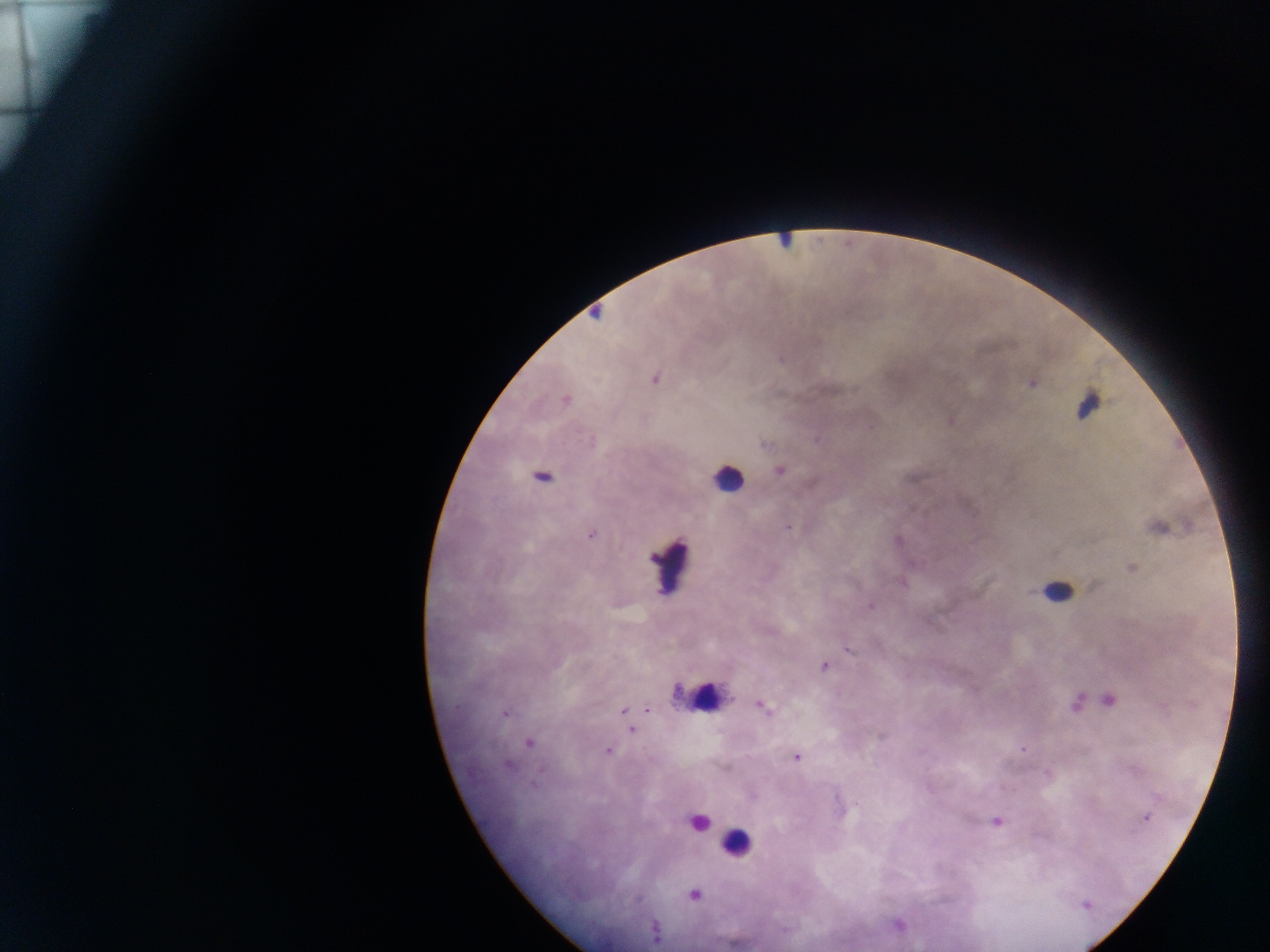 Approximate centers as {x, y} in pixels. Plasmodium parasite locations: {595, 313}, {654, 377}, {1032, 383}, {566, 400}, {949, 420}, {816, 439}, {780, 469}, {541, 477}, {789, 526}, {1158, 526}, {591, 534}, {1131, 567}, {869, 606}, {848, 649}, {824, 666}, {1108, 700}, {1076, 702}, {760, 706}, {646, 708}, {624, 710}, {504, 712}, {627, 718}, {631, 729}, {528, 742}, {1022, 749}, {607, 750}, {796, 756}, {508, 765}, {1047, 773}, {1145, 817}, {995, 820}, {694, 894}, {897, 924}, {655, 933}. Leukocyte locations: {785, 240}, {1088, 405}, {728, 478}, {669, 563}, {1055, 588}, {698, 696}, {696, 821}, {737, 843}. Mobile-phone photograph taken through the microscope. Collected in Ghana. Thick blood smear. One field of view. Image is 1270×952 pixels.